Locate every Plasmodium parasite.
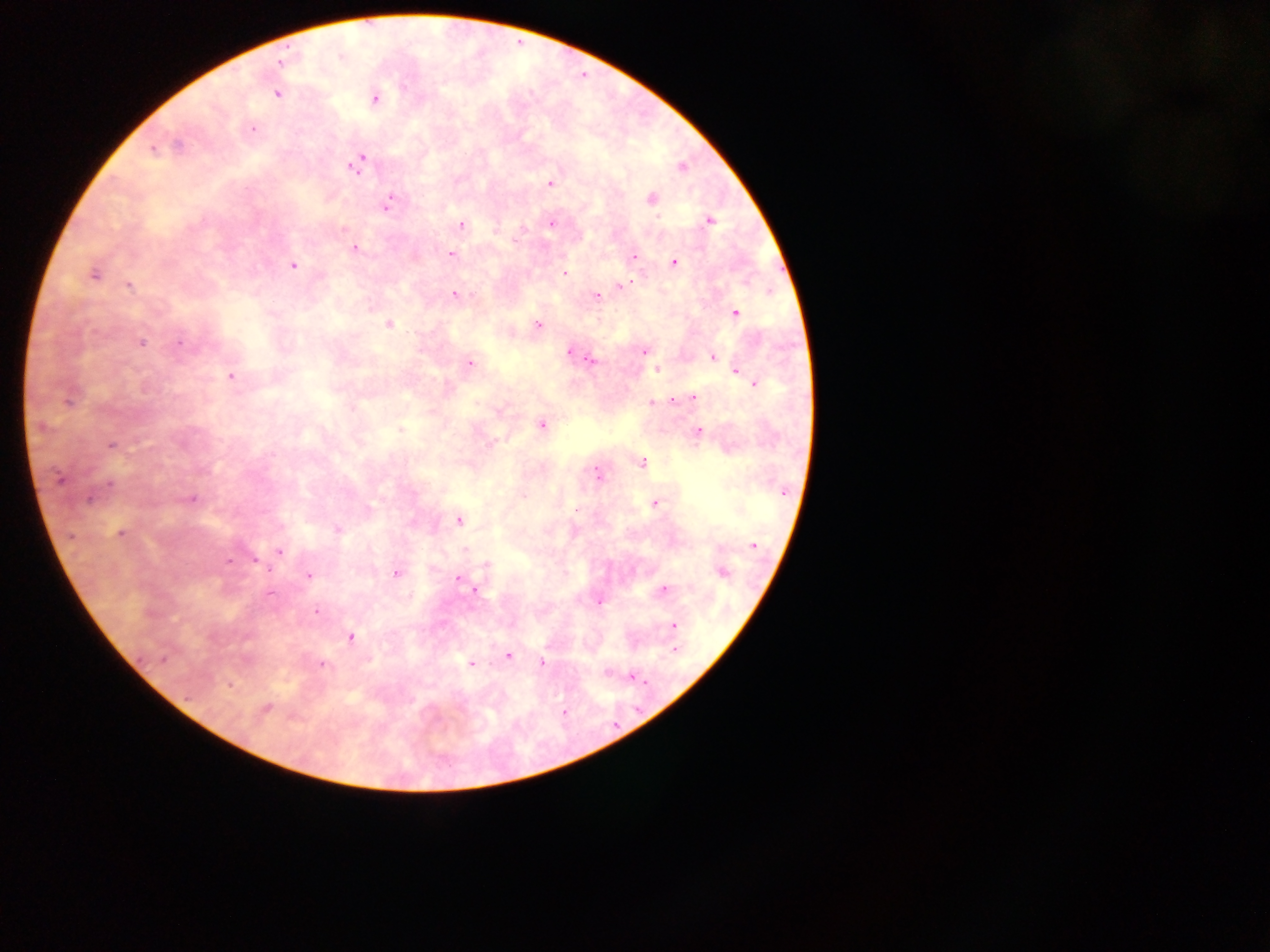

Approximate centers as (x, y) in pixels.
Plasmodium parasites: (277, 94), (375, 99), (253, 129), (178, 144), (153, 149), (356, 165), (682, 167), (551, 183), (651, 198), (389, 202), (710, 221), (552, 223), (461, 224), (355, 248), (450, 254), (634, 257), (674, 262), (292, 265), (565, 273), (94, 275), (624, 285), (128, 286), (455, 294), (596, 297), (735, 313), (389, 325), (538, 325), (181, 342), (142, 343), (570, 351), (645, 351), (713, 357), (591, 360), (470, 363), (656, 369), (737, 372), (231, 376), (754, 384), (693, 398), (674, 400), (68, 402), (652, 403), (542, 426), (41, 427), (400, 430), (699, 432), (111, 445), (641, 462), (598, 473), (59, 479), (110, 484), (90, 498), (192, 499), (654, 503), (575, 510), (459, 520), (338, 529), (120, 533), (753, 545), (465, 549), (279, 551), (229, 561), (486, 564), (396, 573), (722, 573), (308, 575), (459, 580), (469, 586), (664, 589), (476, 591), (270, 594), (600, 602), (317, 611), (673, 626), (352, 637), (675, 650), (508, 657), (162, 659), (542, 662), (471, 664), (321, 665), (606, 673), (633, 676), (229, 685), (266, 708), (564, 712).

capture = mobile-phone photograph through a microscope
preparation = thick blood film
image size = 1270×952 pixels
field of view = single
country = Ghana